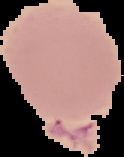
result: no malaria parasites detected
image_type: segmented cell region with the area outside set to black
image_size: 124×157 pixels
preparation: thin blood smear